Report the malaria status of this cell.
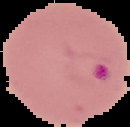

It is parasitized.

image size = 130×127 pixels
preparation = thin blood smear
image type = segmented cell region with the area outside set to black